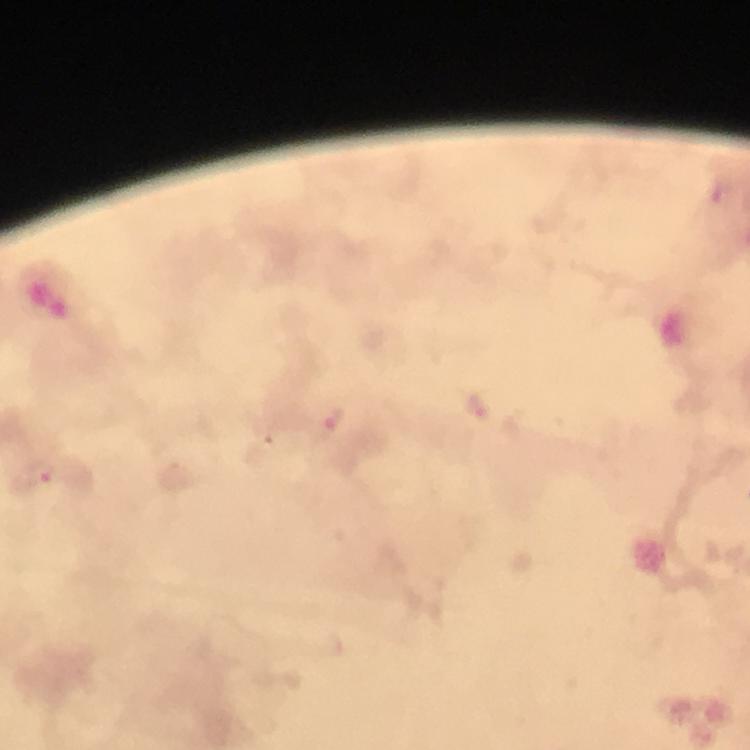

Approximate object centers, in pixels from the top-left corner. Plasmodium parasite locations: (x=722, y=191), (x=477, y=406), (x=332, y=417), (x=40, y=472). Immersion oil applied. Thick blood film. 100x magnification. From a malaria diagnostic workup. Giemsa stain. Photographed through the microscope with a smartphone camera. A crop from one field of view. Image is 750×750 pixels.